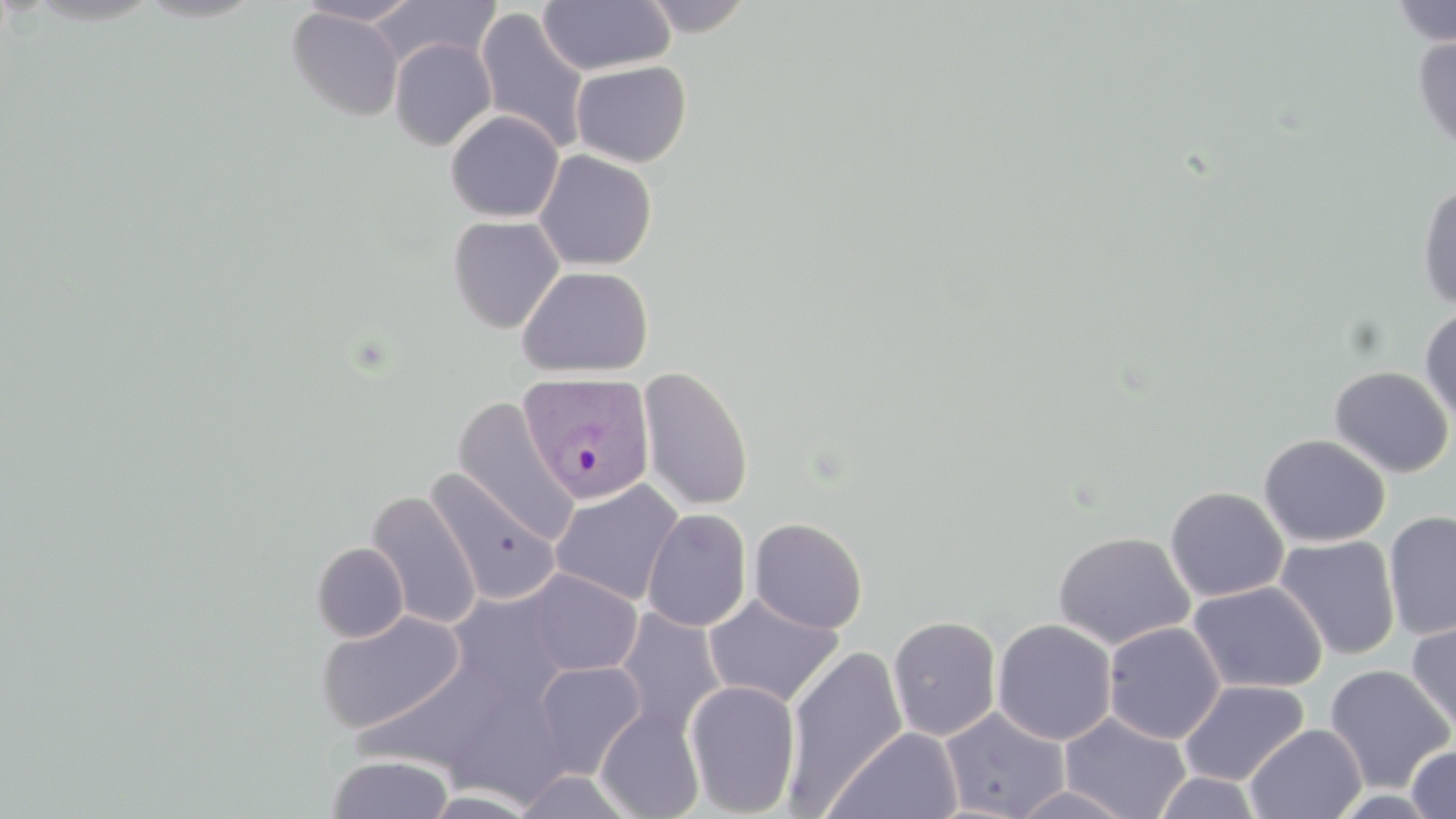

Summary:
  - Coordinate format: approximate bounding boxes as (x1, y1, x2, y2) in pixels
  - Uninfected red blood cell locations: (295, 0, 424, 26), (370, 0, 500, 69), (639, 0, 754, 36), (538, 1, 675, 75), (1387, 1, 1456, 46), (286, 6, 405, 122), (474, 7, 591, 154), (1411, 34, 1456, 155), (389, 37, 496, 150), (570, 60, 692, 167), (445, 110, 564, 222), (534, 149, 656, 270), (1416, 182, 1456, 310), (447, 215, 564, 334), (516, 266, 653, 377), (1419, 306, 1456, 427), (637, 365, 755, 512), (1328, 365, 1454, 478), (451, 396, 579, 544), (1259, 434, 1391, 547), (425, 470, 561, 605), (550, 480, 685, 606), (1164, 485, 1289, 602), (366, 489, 482, 630), (642, 508, 751, 632), (1383, 510, 1456, 640), (749, 517, 868, 633), (1053, 530, 1195, 650), (1274, 535, 1401, 660), (311, 542, 409, 643), (523, 569, 643, 675), (1187, 581, 1328, 694), (448, 587, 574, 707), (703, 593, 845, 708), (614, 607, 727, 737), (315, 610, 465, 733), (887, 615, 1002, 741), (1405, 617, 1456, 739), (992, 618, 1117, 745), (1103, 621, 1225, 744), (783, 645, 908, 812), (353, 660, 512, 775), (533, 660, 646, 779), (1324, 664, 1455, 793), (684, 679, 802, 817), (1179, 680, 1309, 786), (443, 681, 572, 807), (595, 706, 705, 819), (938, 706, 1071, 819), (1059, 712, 1192, 819), (1244, 723, 1366, 819), (826, 725, 963, 819), (1404, 744, 1456, 818), (325, 754, 455, 818), (1152, 771, 1264, 817), (1009, 785, 1139, 818), (424, 789, 543, 817)
  - Plasmodium vivax-infected red blood cell locations: (518, 372, 656, 505)
  - Slide-level diagnosis: Plasmodium vivax
  - Field of view: single
  - Magnification: 1000x
  - Preparation: thin blood smear
  - Modality: light microscopy
  - Stain: May-Grünwald-Giemsa
  - Image size: 1456×819 pixels